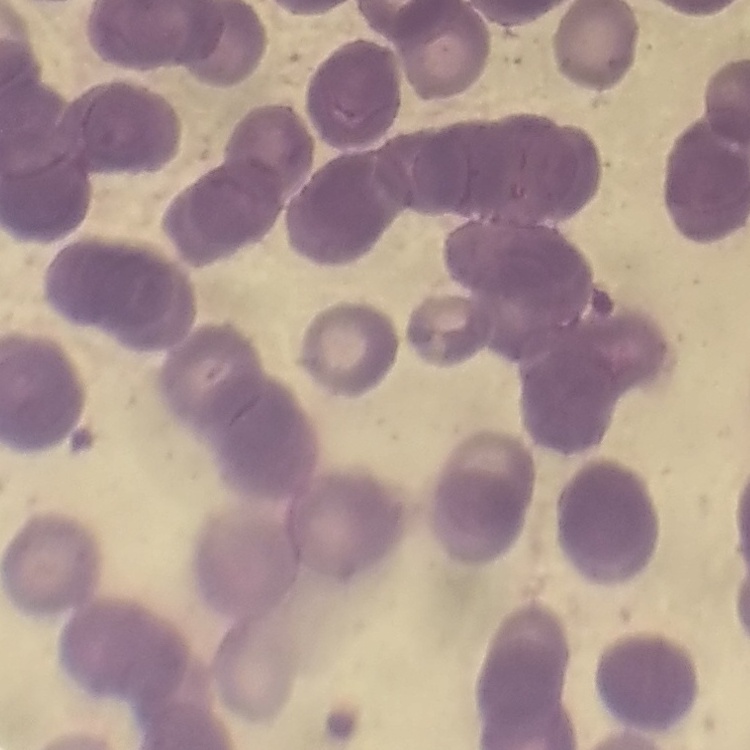 The red blood cells show rouleaux formation. Field's or Giemsa stain. Square crop of a larger photomicrograph. Thin blood film.